Find each white blood cell.
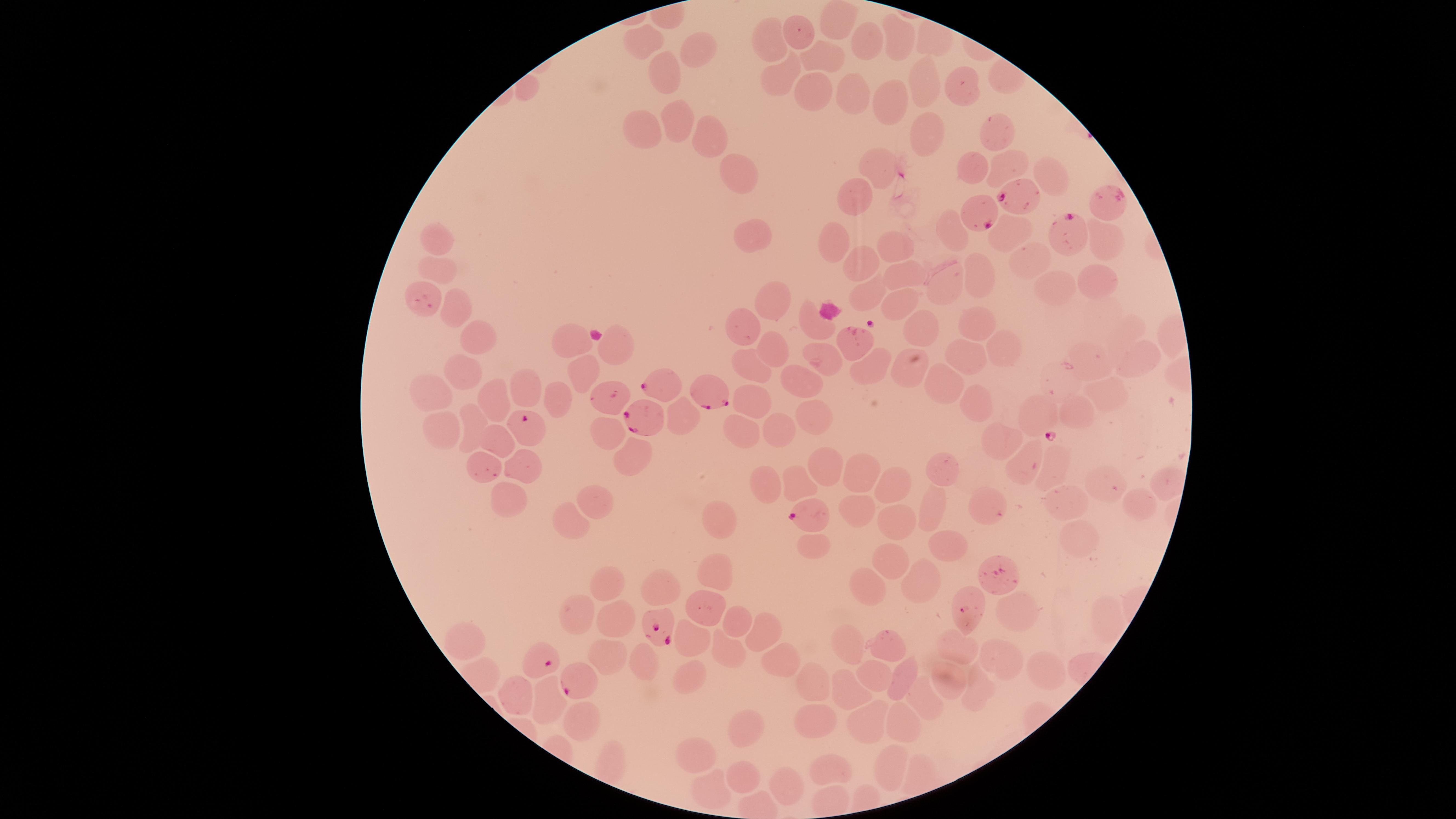
No white blood cells identified.

parasitized red blood cells = approximate marker points as [x, y] in pixels: [1020, 194], [982, 217], [1071, 233], [657, 385], [711, 393], [641, 418], [529, 423], [804, 513], [662, 624], [540, 657], [577, 681]
preparation = thin blood smear
species = Plasmodium falciparum
capture = smartphone photograph through the microscope eyepiece
image size = 1456×819 pixels
uninfected red blood cells = approximate marker points as [x, y] in pixels: [839, 18], [801, 31], [776, 35], [647, 36], [895, 39], [931, 40], [869, 44], [693, 52], [825, 56], [664, 69], [780, 75], [931, 81], [963, 86], [810, 93], [847, 94], [886, 102], [676, 120], [999, 124], [647, 125], [933, 127], [709, 138], [1005, 160], [880, 164], [980, 173], [1047, 173], [736, 177], [860, 199], [749, 231], [1007, 233], [437, 235], [948, 235], [833, 239], [895, 245], [1109, 245], [866, 262], [1027, 267], [438, 272], [901, 273], [987, 277], [1098, 283], [947, 289], [864, 293], [1057, 293], [775, 298], [898, 300], [459, 312], [924, 323], [981, 323], [743, 325], [572, 337], [476, 342], [617, 343], [1005, 345], [772, 348], [968, 354], [913, 356], [1140, 356], [827, 359], [1084, 362], [871, 364], [752, 370], [456, 371], [580, 371], [797, 379], [528, 385], [947, 386], [430, 387], [1106, 392], [497, 393], [751, 395], [555, 397], [978, 399], [1074, 406], [810, 410], [680, 411], [1040, 417], [474, 420], [741, 424], [778, 427], [434, 428], [608, 431], [1004, 433], [494, 445], [636, 451], [1030, 461], [524, 462], [1059, 463], [488, 466], [942, 468], [824, 471], [857, 474], [1109, 478], [1162, 479], [763, 481], [796, 483], [891, 486], [506, 498], [595, 501], [1063, 501], [1138, 504], [929, 510], [983, 510], [853, 511], [575, 514], [721, 522], [893, 523], [1075, 536], [942, 541], [814, 547], [894, 559], [715, 572], [918, 579], [996, 581], [609, 582], [864, 589], [657, 591], [972, 597], [706, 601], [580, 609], [1013, 613], [1102, 618], [614, 620], [733, 620], [761, 629], [693, 635], [455, 640], [888, 641], [846, 643], [729, 644], [961, 648], [601, 652], [640, 656], [776, 656], [1006, 662], [689, 674], [1043, 674], [872, 676], [905, 676], [947, 679], [815, 687], [854, 687], [976, 687], [514, 693], [545, 696], [927, 705], [580, 713], [865, 718], [908, 726], [745, 727], [815, 728], [699, 751], [893, 761], [834, 768], [743, 775], [788, 782], [708, 788]
visible region = circular
field of view = single
presence = malaria parasites seen
stain = Giemsa